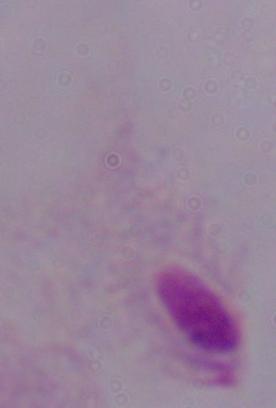

Summary:
  - Modality: photomicrograph
  - Magnification: 1000x
  - Identification: trichomonad